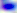
{
  "modality": "photomicrograph",
  "identification": "Toxoplasma gondii",
  "magnification": "400x"
}